Locate and identify every blood parasite.
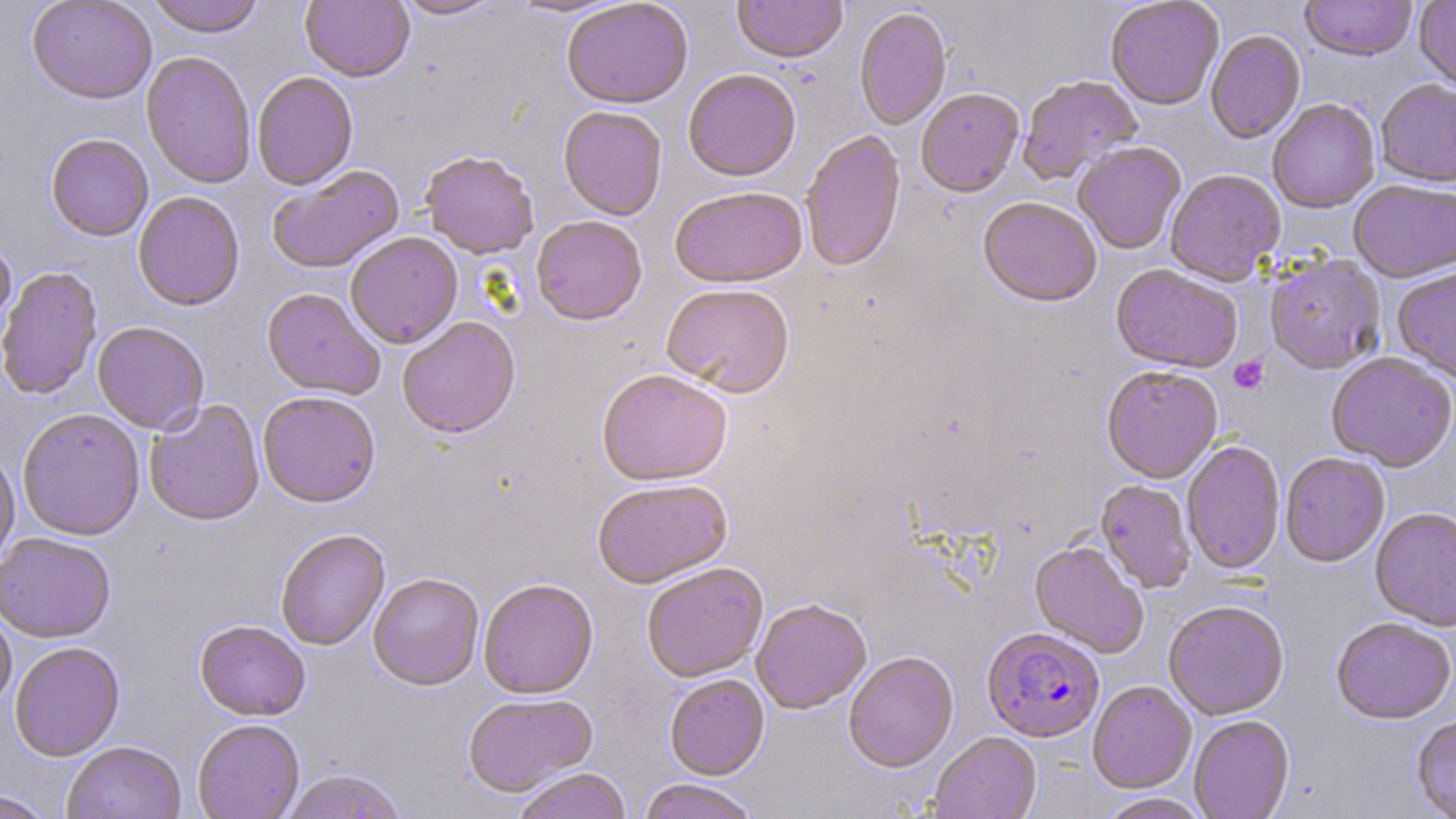
Approximate bounding boxes as named x1/y1/x2/y2 corners in pixels.
Plasmodium falciparum-infected red blood cells: (x1=982, y1=628, x2=1105, y2=743).
No Plasmodium ovale, Plasmodium malariae, Plasmodium vivax, Babesia divergens, or Trypanosoma brucei observed.

Uninfected red blood cell locations: (x1=26, y1=0, x2=157, y2=104), (x1=145, y1=0, x2=265, y2=38), (x1=301, y1=0, x2=414, y2=83), (x1=392, y1=0, x2=504, y2=20), (x1=508, y1=0, x2=630, y2=18), (x1=561, y1=0, x2=693, y2=109), (x1=732, y1=0, x2=847, y2=64), (x1=1105, y1=0, x2=1224, y2=111), (x1=1300, y1=0, x2=1417, y2=63), (x1=1414, y1=0, x2=1456, y2=94), (x1=853, y1=7, x2=952, y2=131), (x1=1205, y1=31, x2=1306, y2=144), (x1=141, y1=51, x2=257, y2=190), (x1=683, y1=68, x2=802, y2=182), (x1=252, y1=71, x2=358, y2=190), (x1=1018, y1=75, x2=1143, y2=186), (x1=1375, y1=80, x2=1456, y2=189), (x1=916, y1=88, x2=1025, y2=198), (x1=1267, y1=99, x2=1380, y2=215), (x1=558, y1=106, x2=667, y2=221), (x1=799, y1=130, x2=906, y2=273), (x1=45, y1=134, x2=154, y2=241), (x1=1073, y1=143, x2=1186, y2=255), (x1=419, y1=150, x2=539, y2=259), (x1=267, y1=164, x2=405, y2=275), (x1=1164, y1=169, x2=1286, y2=287), (x1=1349, y1=181, x2=1456, y2=283), (x1=670, y1=187, x2=808, y2=289), (x1=132, y1=191, x2=245, y2=312), (x1=978, y1=197, x2=1102, y2=309), (x1=531, y1=215, x2=647, y2=326), (x1=345, y1=232, x2=463, y2=349), (x1=0, y1=237, x2=17, y2=351), (x1=1265, y1=254, x2=1386, y2=375), (x1=1110, y1=264, x2=1243, y2=374), (x1=0, y1=266, x2=102, y2=401), (x1=1393, y1=267, x2=1456, y2=384), (x1=660, y1=285, x2=794, y2=398), (x1=261, y1=287, x2=385, y2=400), (x1=396, y1=316, x2=521, y2=439), (x1=92, y1=321, x2=209, y2=434), (x1=1326, y1=353, x2=1455, y2=473), (x1=1101, y1=367, x2=1222, y2=484), (x1=596, y1=369, x2=733, y2=487), (x1=258, y1=391, x2=381, y2=508), (x1=144, y1=399, x2=265, y2=527), (x1=17, y1=409, x2=145, y2=541), (x1=1182, y1=441, x2=1285, y2=575), (x1=0, y1=449, x2=20, y2=568), (x1=1279, y1=454, x2=1390, y2=568), (x1=591, y1=478, x2=733, y2=589), (x1=1095, y1=480, x2=1196, y2=594), (x1=1370, y1=509, x2=1456, y2=632), (x1=276, y1=529, x2=390, y2=651), (x1=0, y1=534, x2=115, y2=643), (x1=1029, y1=540, x2=1149, y2=659), (x1=641, y1=562, x2=768, y2=682), (x1=368, y1=573, x2=484, y2=690), (x1=478, y1=579, x2=598, y2=699), (x1=751, y1=599, x2=871, y2=714), (x1=1163, y1=602, x2=1290, y2=721), (x1=0, y1=607, x2=17, y2=713), (x1=1331, y1=619, x2=1455, y2=726), (x1=194, y1=620, x2=310, y2=721), (x1=9, y1=642, x2=125, y2=762), (x1=843, y1=652, x2=958, y2=773), (x1=664, y1=674, x2=769, y2=780), (x1=1088, y1=681, x2=1197, y2=795), (x1=462, y1=693, x2=598, y2=798), (x1=1189, y1=716, x2=1294, y2=819), (x1=1412, y1=716, x2=1456, y2=819), (x1=192, y1=719, x2=304, y2=819), (x1=929, y1=733, x2=1041, y2=819), (x1=62, y1=741, x2=185, y2=819), (x1=512, y1=768, x2=632, y2=819), (x1=279, y1=770, x2=408, y2=818), (x1=637, y1=779, x2=761, y2=819), (x1=0, y1=791, x2=55, y2=818), (x1=1096, y1=794, x2=1210, y2=819). Platelet locations: (x1=1229, y1=355, x2=1269, y2=395). Slide-level diagnosis: Plasmodium falciparum. May-Grünwald-Giemsa-stained preparation. Captured at 1000x magnification. Thin blood smear. Single field of view. Image is 1456×819 pixels. Light microscopy.